Mark where platelets are.
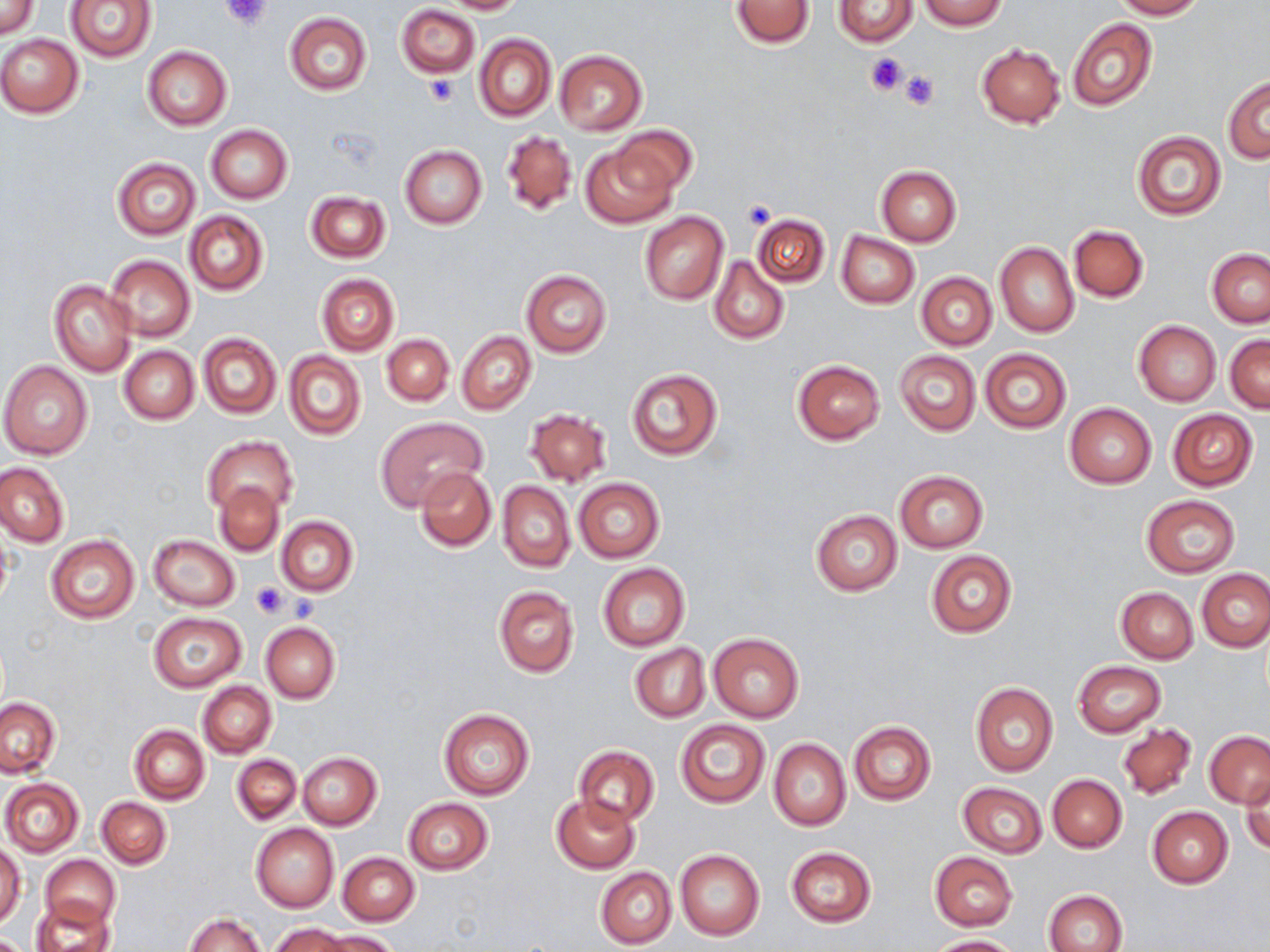
Approximate bounding boxes as (x1, y1, x2, y2) in pixels.
Platelets: (219, 0, 274, 30), (864, 52, 910, 96), (899, 71, 940, 112), (424, 76, 458, 106), (741, 199, 776, 228), (252, 581, 289, 620), (287, 593, 320, 622).

Uninfected red blood cell locations: (0, 0, 38, 38), (439, 0, 525, 14), (729, 0, 816, 50), (833, 0, 919, 46), (920, 0, 1006, 30), (1109, 0, 1204, 20), (66, 1, 156, 62), (396, 5, 480, 77), (284, 13, 371, 95), (1068, 18, 1157, 112), (0, 34, 84, 118), (474, 34, 556, 122), (976, 43, 1066, 129), (141, 46, 232, 130), (553, 50, 647, 135), (1223, 77, 1270, 163), (205, 125, 292, 204), (617, 125, 697, 200), (502, 130, 577, 217), (1131, 130, 1225, 220), (579, 141, 680, 229), (400, 145, 487, 229), (111, 157, 200, 239), (876, 165, 961, 246), (305, 192, 390, 263), (185, 210, 268, 295), (639, 210, 729, 305), (751, 212, 830, 291), (1069, 224, 1148, 302), (836, 231, 919, 309), (995, 242, 1079, 337), (1207, 250, 1270, 327), (105, 255, 195, 342), (710, 256, 789, 345), (520, 270, 612, 357), (917, 272, 996, 349), (316, 273, 399, 355), (49, 279, 138, 377), (1134, 321, 1220, 405), (457, 331, 535, 414), (198, 333, 281, 420), (382, 334, 453, 405), (1225, 334, 1270, 413), (119, 346, 198, 424), (980, 347, 1071, 434), (894, 350, 980, 435), (285, 351, 366, 440), (792, 358, 886, 444), (0, 362, 92, 459), (626, 368, 722, 460), (1066, 402, 1156, 487), (524, 408, 610, 487), (1166, 408, 1258, 491), (379, 418, 487, 510), (202, 437, 296, 515), (0, 463, 69, 547), (415, 466, 495, 551), (894, 470, 988, 552), (573, 477, 664, 562), (498, 481, 574, 571), (214, 482, 285, 556), (1141, 494, 1240, 578), (811, 509, 902, 595), (276, 516, 358, 596), (1, 522, 14, 614), (45, 535, 139, 624), (148, 535, 239, 611), (925, 551, 1017, 638), (597, 562, 690, 651), (1197, 568, 1270, 652), (492, 585, 579, 678), (1116, 587, 1197, 664), (149, 613, 247, 691), (260, 622, 339, 703), (708, 631, 805, 723), (630, 642, 709, 723), (1073, 661, 1166, 737), (197, 682, 276, 757), (970, 682, 1058, 777), (1, 696, 60, 777), (437, 708, 535, 800), (676, 719, 771, 808), (849, 721, 936, 805), (1118, 723, 1197, 799), (130, 725, 209, 804), (1204, 730, 1269, 808), (769, 738, 850, 831), (574, 746, 659, 826), (297, 751, 382, 829), (232, 754, 301, 825), (1047, 774, 1126, 852), (1241, 776, 1269, 857), (1, 778, 83, 856), (958, 782, 1048, 859), (551, 795, 640, 872), (97, 797, 171, 869), (403, 798, 492, 875), (1147, 807, 1232, 887), (250, 823, 339, 913), (1, 843, 25, 929), (786, 847, 875, 927), (675, 848, 764, 941), (337, 852, 419, 926), (929, 852, 1017, 930), (42, 854, 120, 930), (595, 868, 676, 948), (1043, 890, 1126, 952), (33, 901, 115, 952), (185, 913, 263, 952), (269, 923, 348, 952), (316, 930, 398, 952), (928, 934, 1023, 952). Slide-level diagnosis: negative for blood parasites. Single field of view. May-Grünwald-Giemsa-stained preparation. Image is 1270×952 pixels. Optical microscopy. Thin blood smear. 1000x magnification.